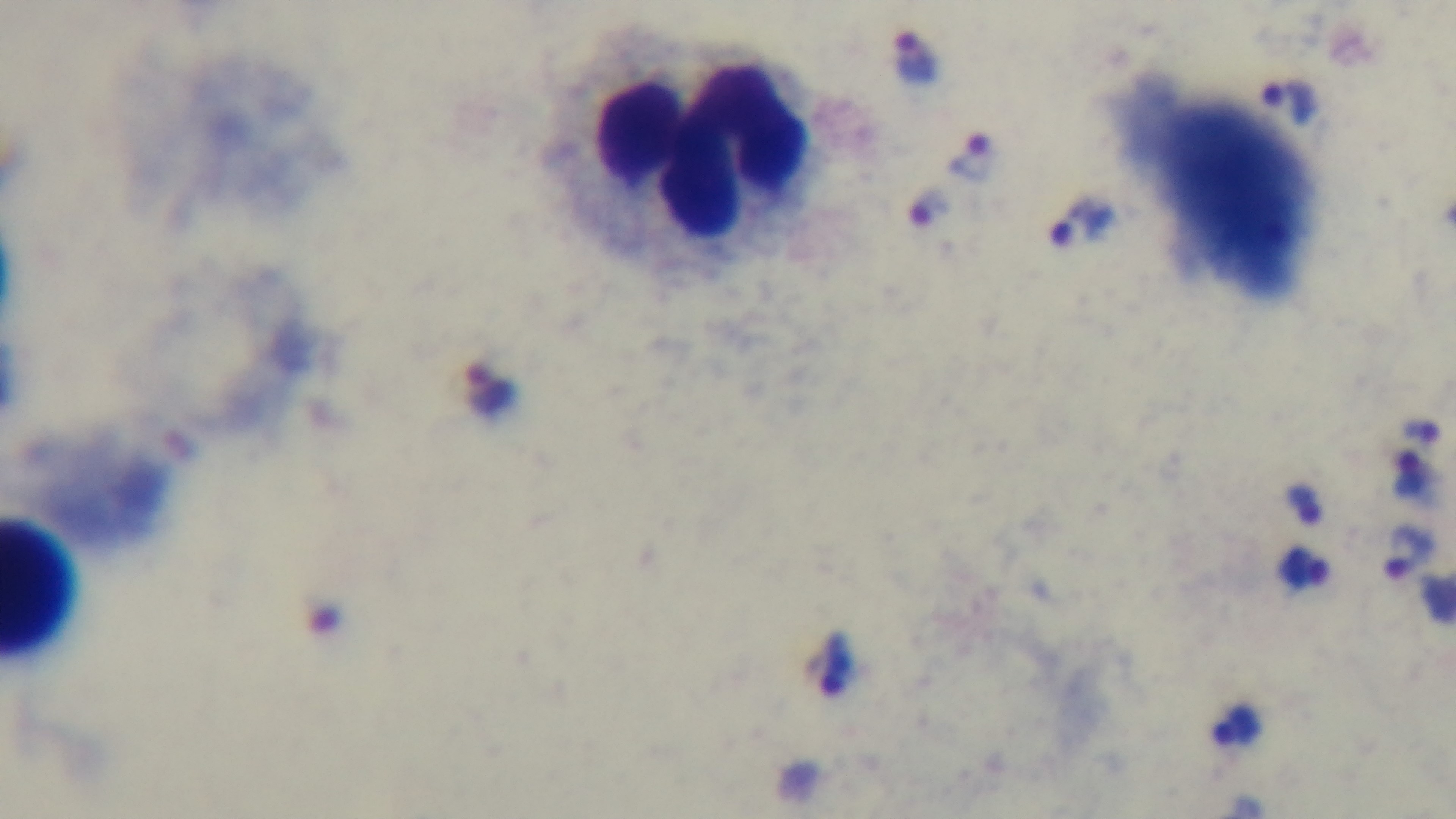
stain = Giemsa
objective = 100x oil immersion
field of view = one from the slide
preparation = thick blood film
malaria status = positive
capture = mounted 4K digital camera
modality = light microscopy